Report the malaria status of this cell.
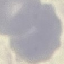

It is uninfected.

Summary:
  - Stain: Giemsa
  - Preparation: thin blood smear
  - Capture: smartphone camera at the microscope eyepiece
  - Image type: cell patch, automatically extracted from a larger field of view and resized to 64 × 64 pixels